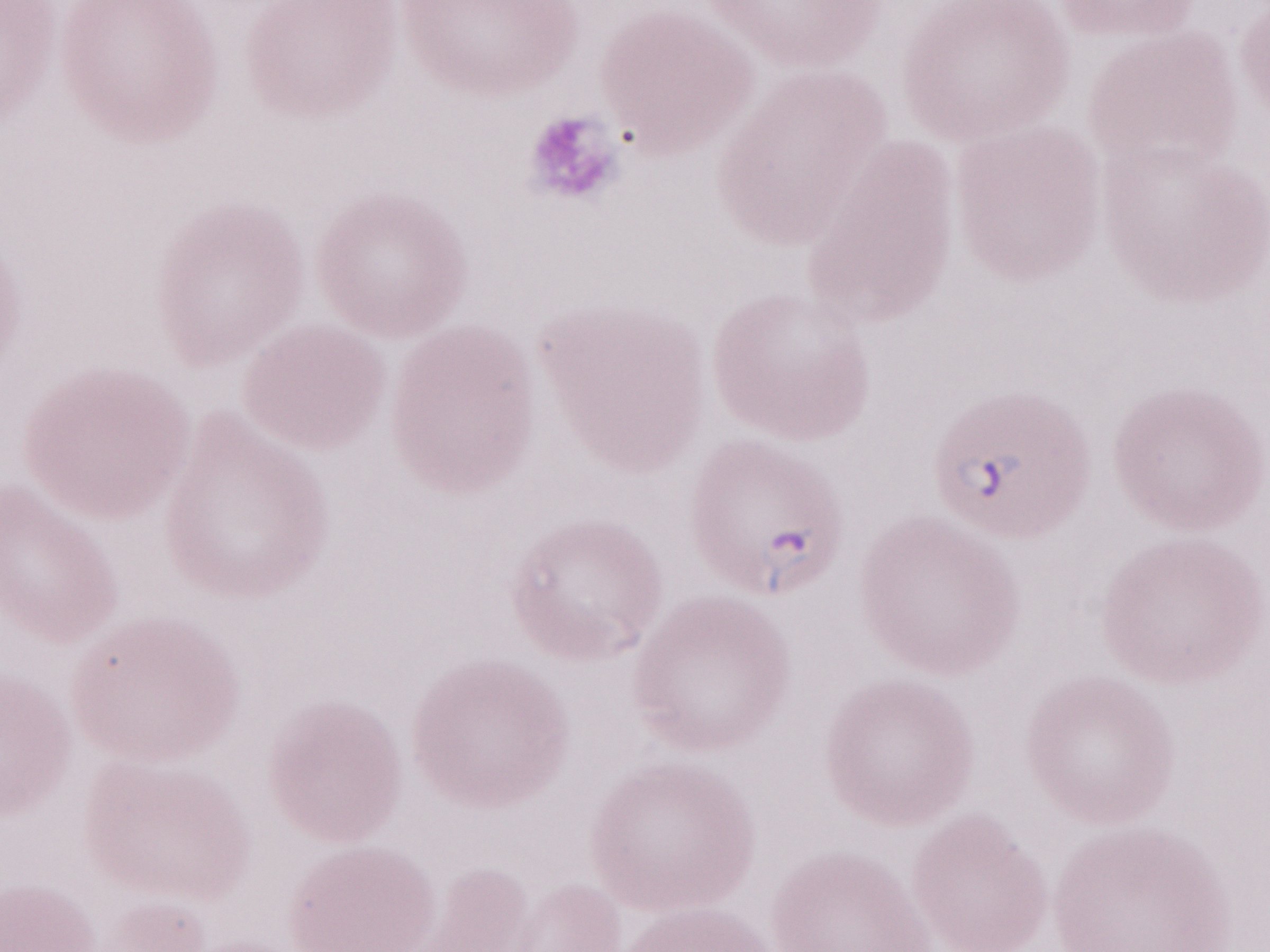
One field of this slide. Patient diagnosis: malaria infection. May-Grünwald-Giemsa stain. Image is 1270×952 pixels. Thin peripheral-blood smear. Olympus BX43 microscope, Olympus DP73 camera. 1,000x magnification.